Assess this cell for malaria.
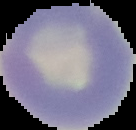
Uninfected.

From a thin blood film. The area outside the segmented cell region is set to black. Image is 136×130 pixels.